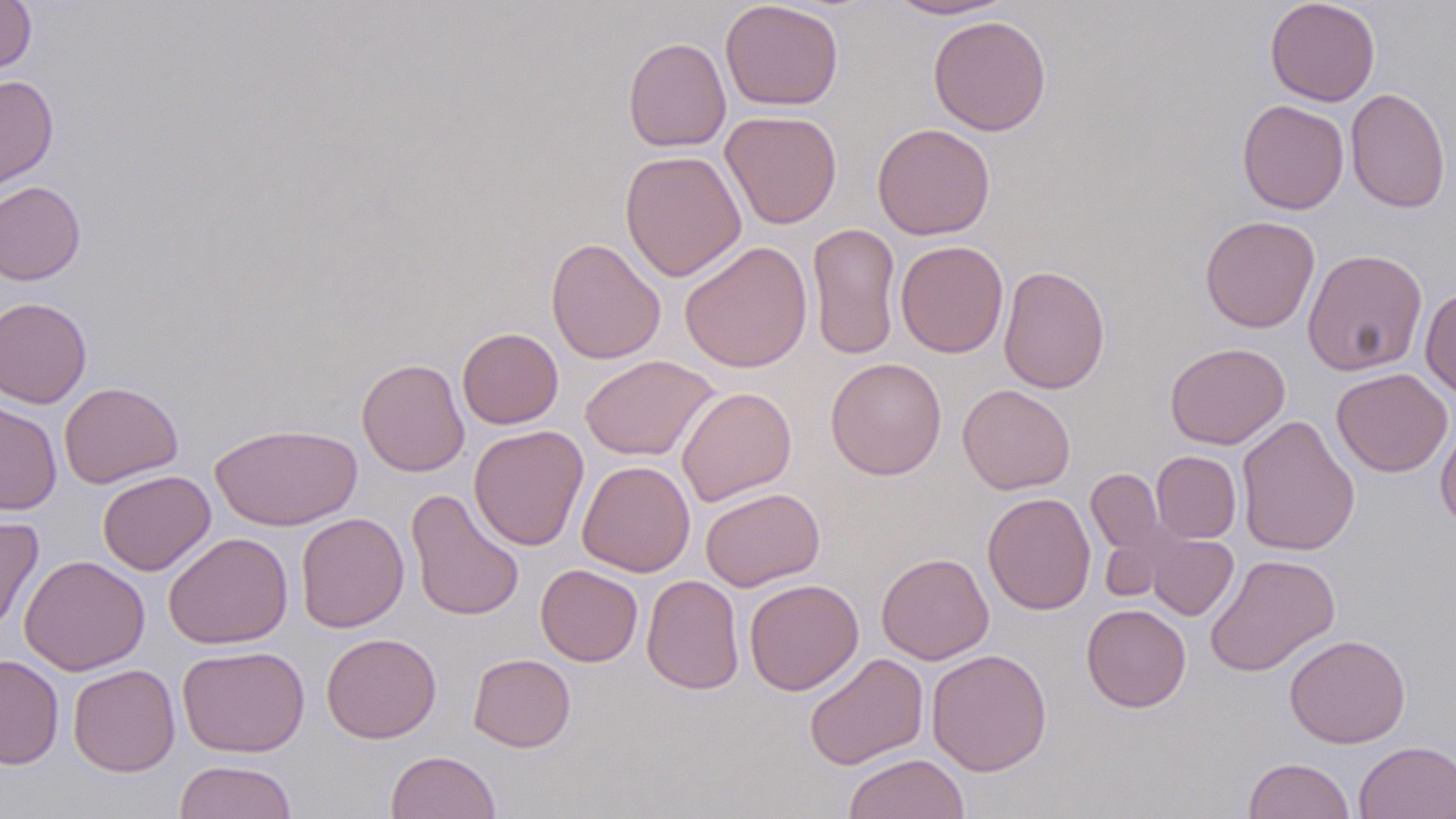

Summary:
  - Coordinate format: approximate bounding boxes as (x1,y1)-(x2,y2) corner pairs in pixels
  - Uninfected red blood cell locations: (0,0)-(37,74), (720,0)-(844,111), (886,0)-(1014,20), (1265,0)-(1380,106), (928,15)-(1051,136), (623,36)-(731,152), (0,75)-(59,192), (1346,87)-(1451,213), (1237,99)-(1349,215), (720,110)-(842,229), (872,122)-(995,240), (620,150)-(746,282), (0,181)-(86,285), (1200,215)-(1320,333), (806,222)-(901,361), (545,237)-(666,364), (895,240)-(1009,358), (679,241)-(813,373), (1302,249)-(1428,376), (998,265)-(1110,394), (1420,287)-(1456,397), (0,297)-(92,408), (457,327)-(563,429), (1165,342)-(1290,449), (580,354)-(720,461), (825,357)-(947,480), (356,358)-(469,477), (1332,368)-(1453,477), (59,382)-(183,488), (957,384)-(1075,494), (676,386)-(797,507), (0,401)-(62,515), (1236,415)-(1360,556), (1435,419)-(1456,532), (210,423)-(361,531), (469,425)-(589,551), (1152,451)-(1242,543), (577,460)-(695,577), (1086,468)-(1166,560), (97,470)-(216,575), (700,487)-(825,591), (405,488)-(525,622), (982,492)-(1096,615), (0,512)-(44,635), (296,512)-(409,633), (1144,530)-(1239,620), (162,532)-(293,650), (876,553)-(994,664), (1204,553)-(1340,677), (19,555)-(150,676), (536,564)-(643,666), (642,574)-(745,694), (743,578)-(864,695), (1081,604)-(1191,712), (321,632)-(441,743), (1284,633)-(1411,748), (177,644)-(310,757), (926,648)-(1052,776), (804,652)-(929,770), (467,653)-(576,752), (0,654)-(64,769), (68,664)-(180,776), (1354,740)-(1456,818), (386,750)-(501,819), (843,753)-(971,819), (1242,757)-(1355,818), (174,760)-(298,819)
  - Slide-level diagnosis: negative for blood parasites
  - Modality: light microscopy
  - Image size: 1456×819 pixels
  - Magnification: 1000x
  - Preparation: thin blood smear
  - Field of view: one of a larger specimen
  - Stain: May-Grünwald-Giemsa